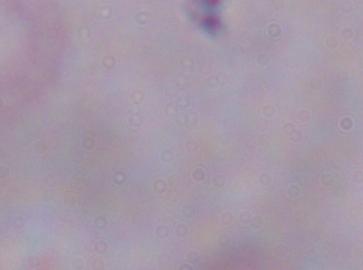
Summary:
  - Identification: trypanosome
  - Magnification: 1000x
  - Modality: micrograph